Name the blood parasite species.
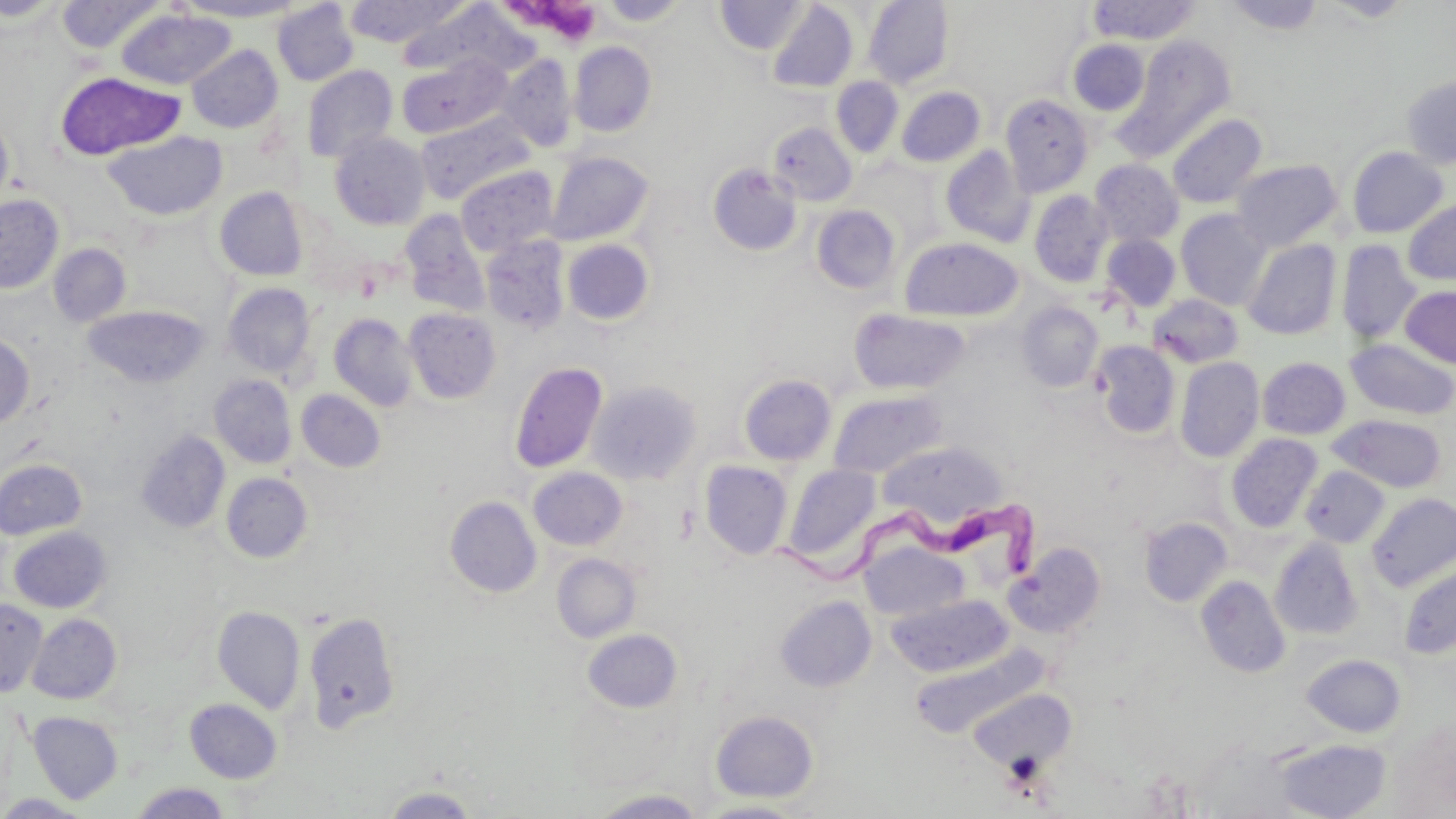

Trypanosoma brucei.

Summary:
  - Coordinate format: approximate bounding boxes as (x1,y1)-(x2,y2) corner pairs in pixels
  - Uninfected red blood cell locations: (0,0)-(68,22), (55,0)-(166,54), (175,0)-(307,21), (344,0)-(472,47), (714,0)-(810,55), (864,0)-(953,89), (1087,0)-(1201,44), (1222,0)-(1327,34), (1321,0)-(1417,23), (596,1)-(693,26), (272,2)-(358,86), (767,2)-(858,93), (395,3)-(534,81), (117,9)-(236,90), (1118,35)-(1236,155), (1068,40)-(1149,115), (569,42)-(656,136), (187,45)-(282,133), (497,54)-(578,152), (397,55)-(512,140), (302,65)-(398,162), (56,72)-(185,161), (1401,75)-(1456,170), (831,77)-(903,157), (896,87)-(985,167), (1000,94)-(1093,195), (0,111)-(14,216), (416,113)-(534,205), (1166,113)-(1267,209), (768,122)-(857,206), (103,131)-(227,221), (329,131)-(430,230), (939,145)-(1034,248), (1346,146)-(1449,238), (546,152)-(653,245), (1090,159)-(1184,247), (1230,159)-(1343,251), (708,164)-(802,255), (455,166)-(558,257), (214,187)-(308,281), (1029,190)-(1113,288), (0,194)-(64,294), (1402,198)-(1456,286), (811,205)-(901,294), (1175,209)-(1272,310), (399,210)-(491,316), (1100,234)-(1182,313), (481,236)-(570,334), (899,237)-(1023,322), (562,239)-(654,324), (1242,239)-(1341,340), (1336,240)-(1421,346), (48,243)-(131,326), (223,283)-(316,378), (1400,285)-(1456,368), (1147,293)-(1243,368), (1017,302)-(1104,392), (83,307)-(210,387), (403,308)-(500,404), (849,308)-(969,395), (329,313)-(418,411), (0,334)-(34,428), (1345,339)-(1456,420), (1092,341)-(1180,439), (1256,353)-(1456,433), (1175,357)-(1264,462), (1257,357)-(1350,439), (509,361)-(608,473), (739,373)-(837,465), (209,374)-(297,468), (587,380)-(702,485), (295,389)-(386,472), (828,389)-(948,478), (1328,414)-(1448,493), (137,431)-(230,532), (1227,434)-(1323,532), (877,441)-(1005,527), (0,458)-(87,540), (699,460)-(793,559), (782,463)-(882,566), (1300,465)-(1390,548), (528,467)-(627,550), (221,472)-(313,563), (1368,492)-(1456,591), (445,495)-(542,598), (1139,517)-(1232,606), (9,526)-(111,613), (1269,537)-(1363,640), (862,541)-(968,621), (1007,542)-(1106,638), (551,553)-(641,643), (1399,563)-(1456,659), (1196,576)-(1290,678), (886,594)-(1011,677), (775,596)-(876,691), (0,599)-(47,697), (212,606)-(306,713), (303,610)-(401,734), (28,614)-(121,704), (582,628)-(682,713), (908,645)-(1044,738), (1302,654)-(1406,737), (969,686)-(1077,770), (184,698)-(282,783), (710,710)-(818,803), (28,711)-(123,803), (1274,739)-(1391,819), (129,782)-(232,819), (380,786)-(480,818), (591,789)-(708,818), (0,794)-(94,818), (694,800)-(812,818)
  - Platelet locations: (511,3)-(606,47)
  - Trypanosoma brucei locations: (768,491)-(1043,604)
  - Modality: light microscopy
  - Magnification: 1000x
  - Stain: May-Grünwald-Giemsa
  - Field of view: one of a larger specimen
  - Preparation: thin blood smear
  - Image size: 1456×819 pixels